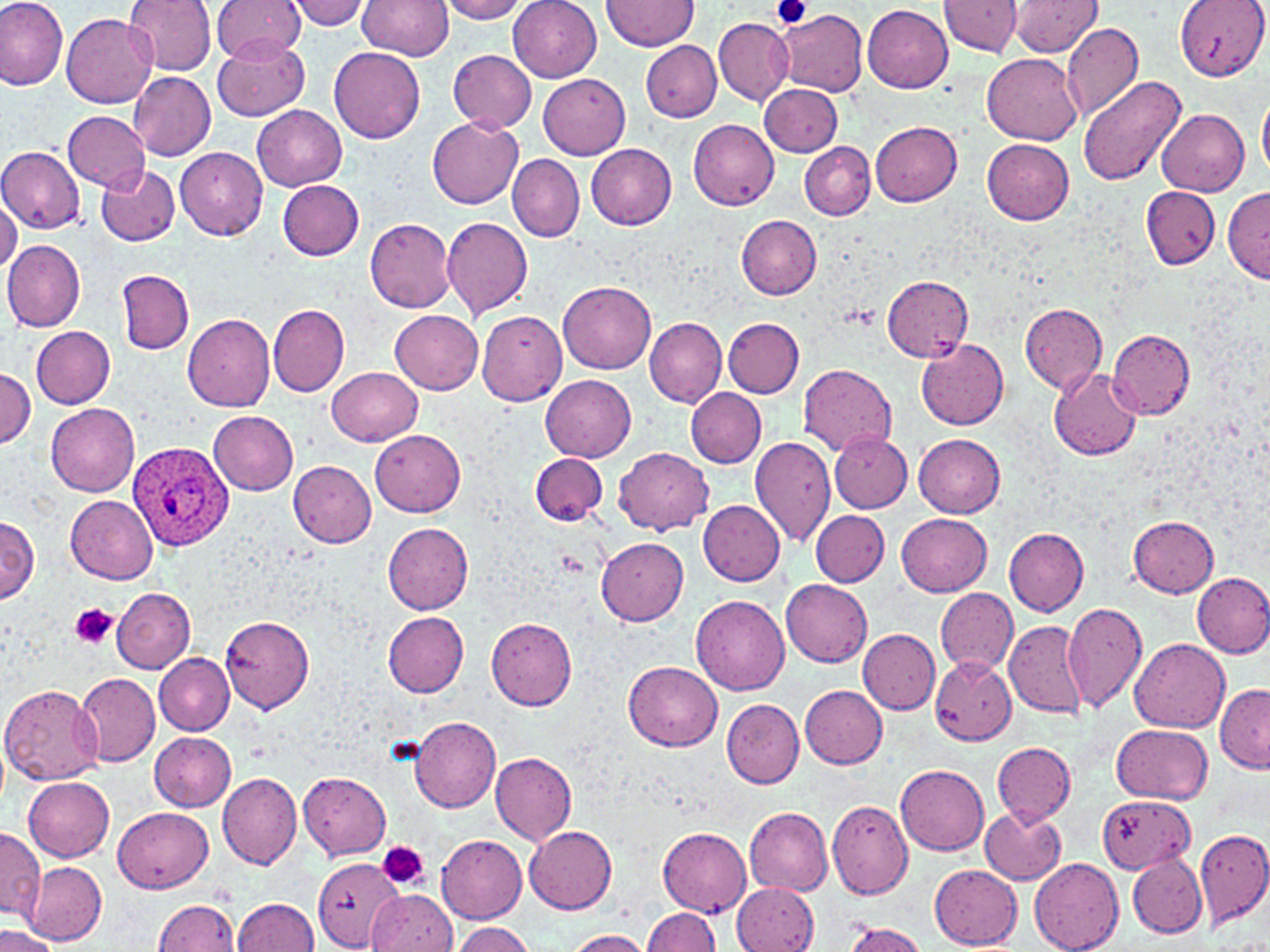

Summary:
  - Coordinate format: approximate bounding boxes as named x1/y1/x2/y2 corners in pixels
  - Plasmodium ovale-infected red blood cell locations: (x1=126, y1=438, x2=233, y2=552)
  - Platelet locations: (x1=773, y1=0, x2=809, y2=29), (x1=71, y1=603, x2=116, y2=650), (x1=377, y1=841, x2=429, y2=891)
  - Uninfected red blood cell locations: (x1=0, y1=0, x2=69, y2=90), (x1=123, y1=0, x2=216, y2=74), (x1=214, y1=0, x2=308, y2=64), (x1=284, y1=0, x2=373, y2=30), (x1=357, y1=0, x2=453, y2=59), (x1=439, y1=0, x2=530, y2=23), (x1=508, y1=0, x2=601, y2=82), (x1=603, y1=0, x2=699, y2=51), (x1=1010, y1=0, x2=1100, y2=56), (x1=1176, y1=0, x2=1267, y2=81), (x1=940, y1=1, x2=1021, y2=57), (x1=863, y1=5, x2=953, y2=93), (x1=776, y1=8, x2=868, y2=97), (x1=62, y1=13, x2=157, y2=107), (x1=713, y1=15, x2=793, y2=105), (x1=1062, y1=21, x2=1145, y2=124), (x1=212, y1=33, x2=310, y2=121), (x1=641, y1=41, x2=721, y2=122), (x1=329, y1=48, x2=425, y2=143), (x1=448, y1=50, x2=537, y2=131), (x1=983, y1=53, x2=1084, y2=144), (x1=128, y1=70, x2=215, y2=160), (x1=537, y1=74, x2=630, y2=160), (x1=1077, y1=76, x2=1187, y2=190), (x1=759, y1=83, x2=842, y2=157), (x1=1259, y1=95, x2=1270, y2=176), (x1=251, y1=103, x2=347, y2=190), (x1=1156, y1=108, x2=1250, y2=196), (x1=63, y1=110, x2=150, y2=191), (x1=428, y1=117, x2=524, y2=209), (x1=688, y1=119, x2=780, y2=210), (x1=871, y1=121, x2=962, y2=206), (x1=982, y1=138, x2=1075, y2=225), (x1=800, y1=140, x2=875, y2=220), (x1=585, y1=143, x2=677, y2=229), (x1=0, y1=146, x2=85, y2=233), (x1=175, y1=147, x2=268, y2=240), (x1=507, y1=154, x2=584, y2=241), (x1=95, y1=163, x2=180, y2=246), (x1=278, y1=180, x2=365, y2=261), (x1=1222, y1=185, x2=1270, y2=282), (x1=1140, y1=186, x2=1221, y2=268), (x1=0, y1=193, x2=22, y2=275), (x1=441, y1=215, x2=534, y2=319), (x1=736, y1=215, x2=821, y2=299), (x1=364, y1=217, x2=457, y2=311), (x1=2, y1=240, x2=85, y2=332), (x1=117, y1=270, x2=193, y2=353), (x1=880, y1=276, x2=973, y2=360), (x1=559, y1=281, x2=656, y2=375), (x1=267, y1=303, x2=350, y2=396), (x1=1019, y1=305, x2=1107, y2=393), (x1=476, y1=309, x2=567, y2=407), (x1=391, y1=310, x2=482, y2=393), (x1=182, y1=311, x2=275, y2=411), (x1=645, y1=316, x2=727, y2=407), (x1=723, y1=317, x2=805, y2=398), (x1=31, y1=326, x2=115, y2=409), (x1=1108, y1=329, x2=1196, y2=419), (x1=916, y1=338, x2=1009, y2=431), (x1=798, y1=364, x2=897, y2=457), (x1=1, y1=366, x2=35, y2=449), (x1=328, y1=367, x2=423, y2=445), (x1=1049, y1=367, x2=1140, y2=460), (x1=541, y1=375, x2=636, y2=462), (x1=686, y1=388, x2=766, y2=467), (x1=46, y1=403, x2=140, y2=497), (x1=207, y1=410, x2=299, y2=495), (x1=370, y1=429, x2=466, y2=517), (x1=829, y1=431, x2=911, y2=512), (x1=913, y1=432, x2=1006, y2=518), (x1=750, y1=435, x2=837, y2=547), (x1=614, y1=448, x2=713, y2=534), (x1=531, y1=453, x2=608, y2=526), (x1=287, y1=460, x2=377, y2=547), (x1=65, y1=495, x2=159, y2=585), (x1=698, y1=499, x2=785, y2=586), (x1=811, y1=510, x2=890, y2=587), (x1=896, y1=511, x2=993, y2=596), (x1=1130, y1=515, x2=1219, y2=596), (x1=0, y1=517, x2=39, y2=604), (x1=382, y1=523, x2=473, y2=614), (x1=1004, y1=528, x2=1089, y2=615), (x1=597, y1=538, x2=690, y2=626), (x1=1192, y1=572, x2=1270, y2=658), (x1=782, y1=579, x2=873, y2=669), (x1=935, y1=586, x2=1018, y2=677), (x1=111, y1=588, x2=195, y2=672), (x1=691, y1=596, x2=790, y2=695), (x1=1061, y1=602, x2=1148, y2=713), (x1=382, y1=612, x2=468, y2=697), (x1=485, y1=614, x2=577, y2=711), (x1=220, y1=617, x2=315, y2=713), (x1=1004, y1=619, x2=1088, y2=720), (x1=859, y1=629, x2=940, y2=714), (x1=1131, y1=639, x2=1231, y2=733), (x1=154, y1=653, x2=235, y2=735), (x1=929, y1=657, x2=1016, y2=746), (x1=623, y1=661, x2=723, y2=751), (x1=75, y1=674, x2=161, y2=766), (x1=0, y1=683, x2=105, y2=785), (x1=1215, y1=683, x2=1270, y2=772), (x1=800, y1=686, x2=888, y2=769), (x1=722, y1=698, x2=805, y2=788), (x1=410, y1=716, x2=501, y2=812), (x1=1111, y1=724, x2=1213, y2=803), (x1=150, y1=732, x2=237, y2=812), (x1=0, y1=736, x2=9, y2=808), (x1=993, y1=742, x2=1075, y2=825), (x1=491, y1=753, x2=577, y2=844), (x1=896, y1=764, x2=989, y2=855), (x1=217, y1=769, x2=302, y2=870), (x1=300, y1=773, x2=391, y2=859), (x1=23, y1=777, x2=115, y2=862), (x1=1096, y1=795, x2=1194, y2=873), (x1=826, y1=799, x2=914, y2=901), (x1=979, y1=805, x2=1067, y2=886), (x1=114, y1=807, x2=212, y2=894), (x1=745, y1=808, x2=833, y2=895), (x1=524, y1=825, x2=618, y2=913), (x1=658, y1=827, x2=752, y2=916), (x1=1194, y1=827, x2=1270, y2=930), (x1=0, y1=829, x2=44, y2=921), (x1=437, y1=834, x2=527, y2=923), (x1=1128, y1=854, x2=1207, y2=938), (x1=312, y1=857, x2=407, y2=950), (x1=1030, y1=859, x2=1124, y2=952), (x1=24, y1=863, x2=106, y2=944), (x1=929, y1=865, x2=1022, y2=949), (x1=733, y1=882, x2=819, y2=952), (x1=369, y1=891, x2=458, y2=952), (x1=232, y1=897, x2=320, y2=951), (x1=152, y1=899, x2=241, y2=951), (x1=641, y1=906, x2=719, y2=952), (x1=451, y1=922, x2=534, y2=952), (x1=839, y1=922, x2=929, y2=952), (x1=0, y1=926, x2=61, y2=952), (x1=563, y1=929, x2=653, y2=951)
  - Slide-level diagnosis: Plasmodium ovale
  - Modality: optical microscopy
  - Image size: 1270×952 pixels
  - Stain: May-Grünwald-Giemsa
  - Magnification: 1000x
  - Field of view: one of a larger specimen
  - Preparation: thin blood film